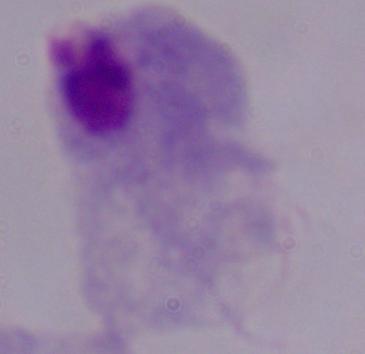
identification: trichomonad
magnification: 1000x
modality: photomicrograph